Identify the parasite.
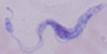
A trypanosome.

magnification = 1000x
modality = micrograph